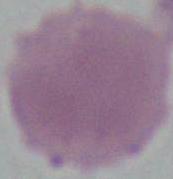
identification = erythrocyte
magnification = 1000x
modality = micrograph